Give the extent of all Plasmodium falciparum-infected red blood cells.
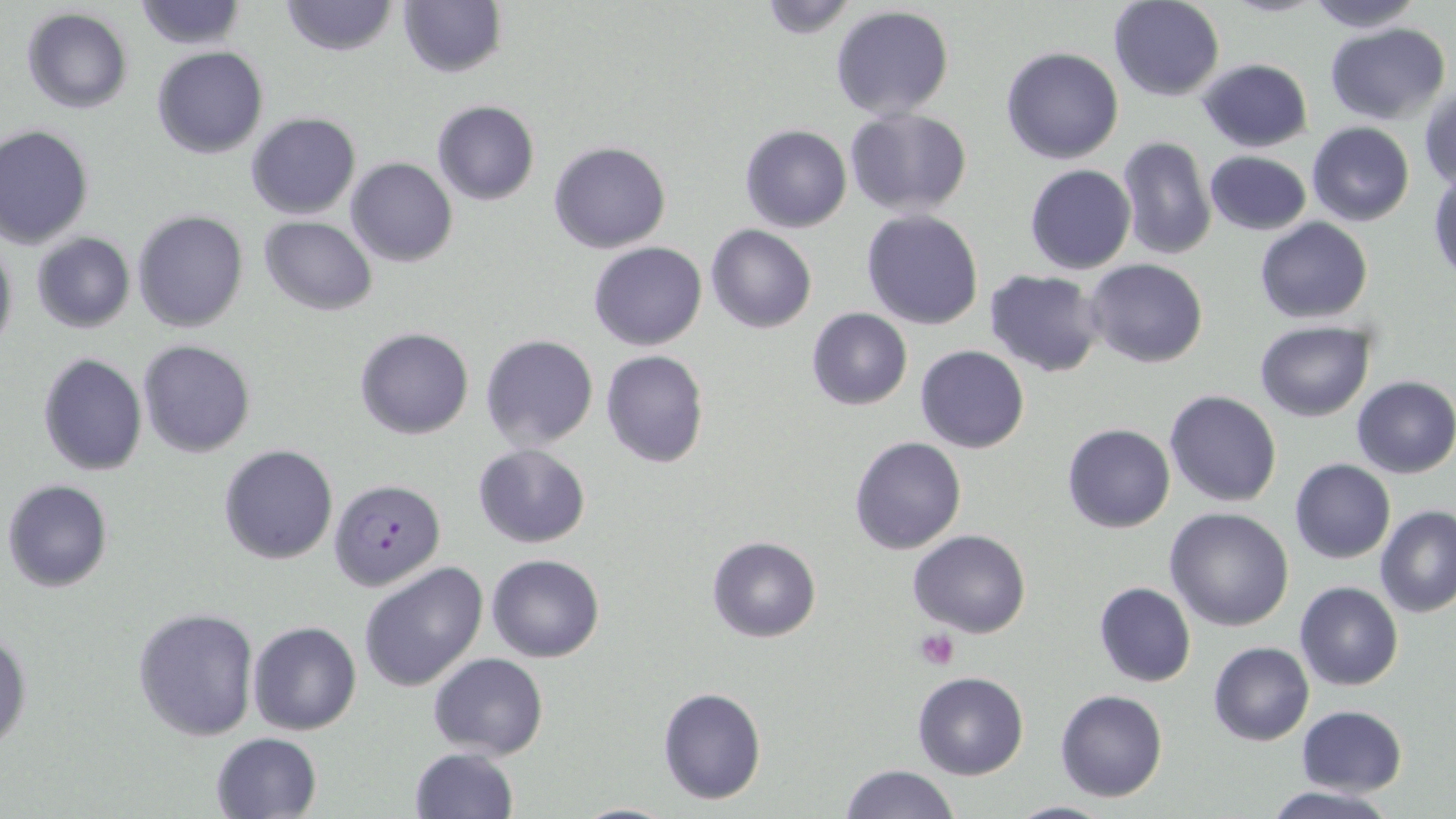
Approximate bounding boxes as (x1, y1, x2, y2) in pixels.
Plasmodium falciparum-infected red blood cells: (328, 477, 446, 593).

{
  "slide_level_diagnosis": "Plasmodium falciparum",
  "stain": "May-Grünwald-Giemsa",
  "preparation": "thin blood smear",
  "magnification": "1000x",
  "image_size": "1456×819 pixels",
  "modality": "optical microscopy",
  "field_of_view": "one of a larger specimen",
  "uninfected_red_blood_cell_locations": "approximate bounding boxes as (x1, y1, x2, y2) in pixels: (278, 0, 399, 57), (1303, 0, 1423, 33), (132, 1, 248, 50), (754, 1, 861, 38), (1108, 1, 1225, 102), (397, 2, 506, 77), (830, 5, 955, 122), (21, 8, 133, 113), (1324, 22, 1452, 126), (152, 46, 269, 159), (1001, 47, 1123, 164), (1196, 59, 1313, 153), (1419, 83, 1455, 191), (431, 101, 540, 205), (845, 110, 973, 217), (246, 112, 360, 221), (1306, 122, 1414, 226), (0, 125, 95, 248), (740, 125, 852, 232), (1116, 134, 1215, 261), (548, 140, 671, 253), (1203, 149, 1312, 235), (345, 157, 457, 268), (1024, 163, 1137, 275), (1429, 172, 1456, 282), (133, 209, 248, 331), (862, 210, 983, 329), (260, 218, 378, 314), (1255, 218, 1374, 323), (706, 225, 816, 333), (29, 232, 135, 333), (0, 233, 17, 359), (589, 241, 706, 351), (1084, 259, 1209, 369), (984, 269, 1106, 378), (805, 307, 913, 411), (1254, 321, 1375, 421), (355, 327, 473, 439), (480, 334, 599, 452), (139, 340, 255, 457), (915, 344, 1029, 454), (600, 349, 710, 468), (38, 352, 148, 475), (1353, 376, 1455, 478), (1164, 389, 1282, 507), (1062, 422, 1174, 533), (848, 436, 965, 556), (218, 444, 339, 565), (473, 444, 590, 548), (1289, 459, 1395, 564), (3, 478, 115, 594), (1374, 505, 1456, 618), (1165, 507, 1295, 630), (907, 530, 1032, 638), (706, 535, 822, 641), (486, 553, 604, 662), (358, 560, 489, 692), (1093, 581, 1196, 687), (1295, 582, 1403, 690), (132, 605, 259, 742), (248, 621, 362, 734), (0, 628, 32, 754), (1208, 641, 1314, 746), (427, 652, 548, 760), (912, 672, 1029, 781), (657, 686, 767, 804), (1055, 689, 1169, 802), (1296, 705, 1407, 796), (210, 732, 324, 819), (407, 747, 520, 818), (838, 764, 960, 819), (1262, 785, 1397, 818), (1001, 800, 1121, 819), (564, 801, 686, 819)",
  "platelet_locations": "approximate bounding boxes as (x1, y1, x2, y2) in pixels: (913, 628, 960, 670)"
}